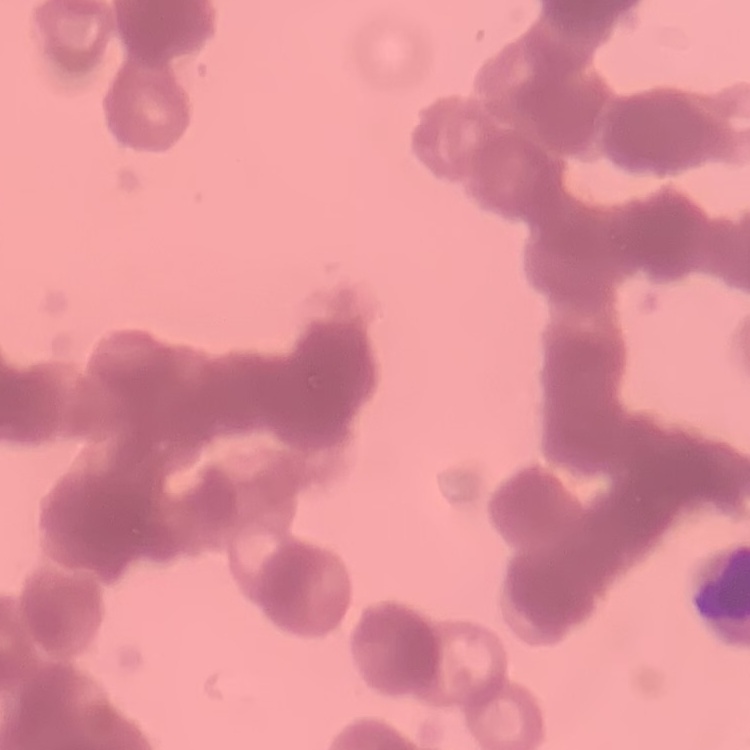 The red blood cells exhibit rouleaux formation. Thin peripheral smear. Stained with either Field's or Giemsa. One tile cut from a larger photomicrograph.